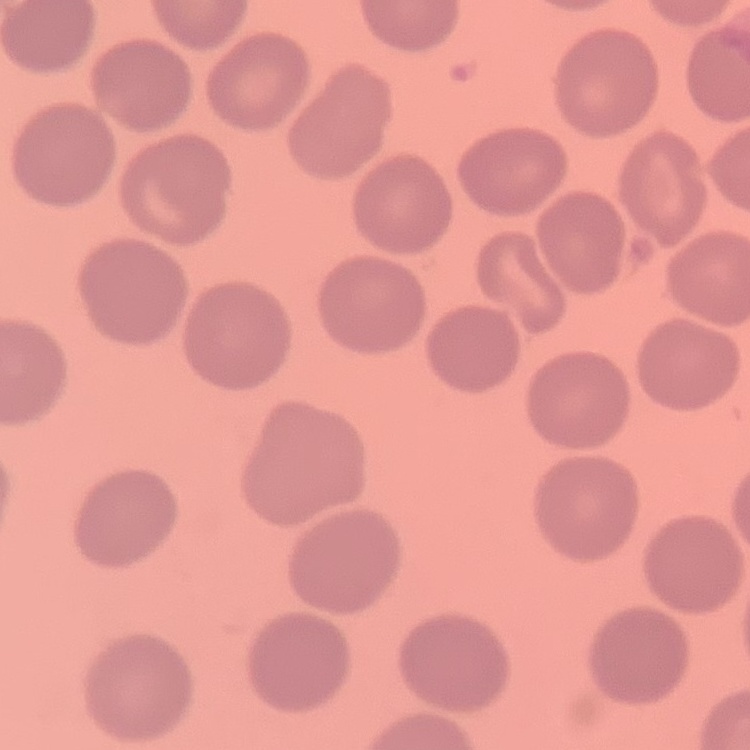

{
  "erythrocyte_morphology": "no rouleaux formation",
  "stain": "Field's or Giemsa",
  "image_type": "square crop of a larger photomicrograph",
  "preparation": "thin peripheral smear"
}